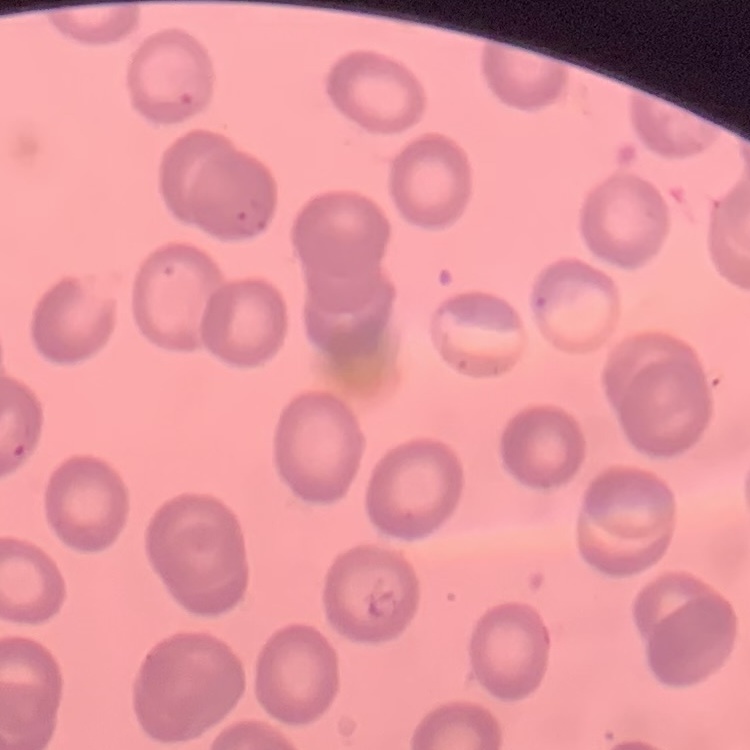

Summary:
  - Erythrocyte morphology: no rouleaux formation
  - Image type: square crop of a larger photomicrograph
  - Stain: Field's or Giemsa
  - Preparation: thin blood smear